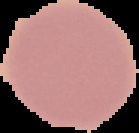
Malaria status: uninfected. Segmented cell region on a black background. From a thin blood smear. Image is 139×133 pixels.